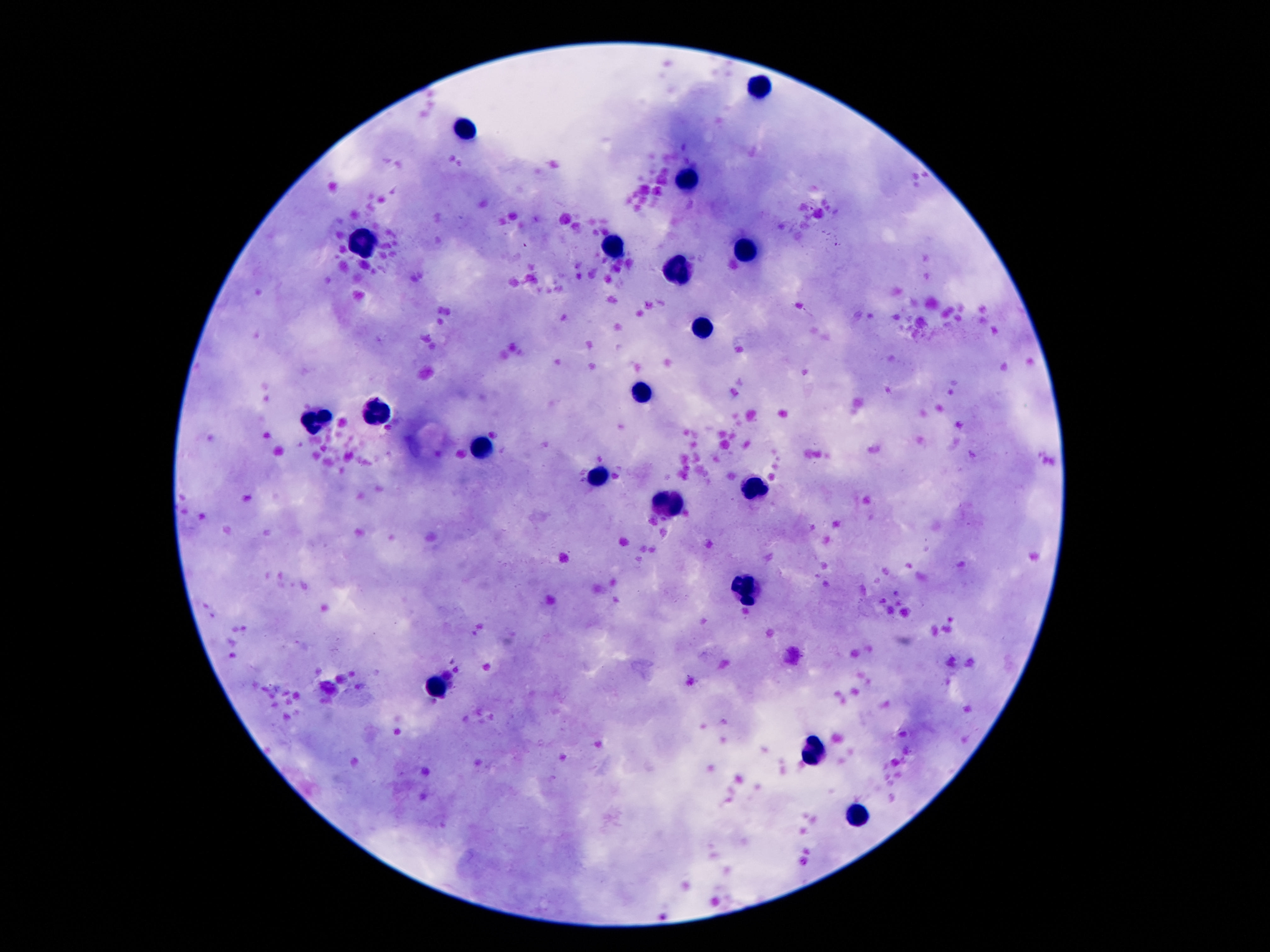
leukocyte_locations: 'approximate object centers, in pixels from the top-left corner: (x=763, y=87), (x=466, y=127), (x=688, y=178), (x=358, y=244), (x=616, y=248), (x=746, y=248), (x=679, y=271), (x=703, y=330), (x=643, y=391), (x=379, y=407), (x=317, y=420), (x=478, y=450), (x=595, y=479), (x=749, y=488), (x=672, y=503), (x=744, y=587), (x=441, y=686), (x=809, y=750), (x=854, y=815)'
field_of_view: one from this slide
magnification: 100x
patient_malaria_status: uninfected
stain: Giemsa
image_size: 1270×952 pixels
preparation: thick peripheral-blood smear
capture: smartphone camera through the microscope eyepiece